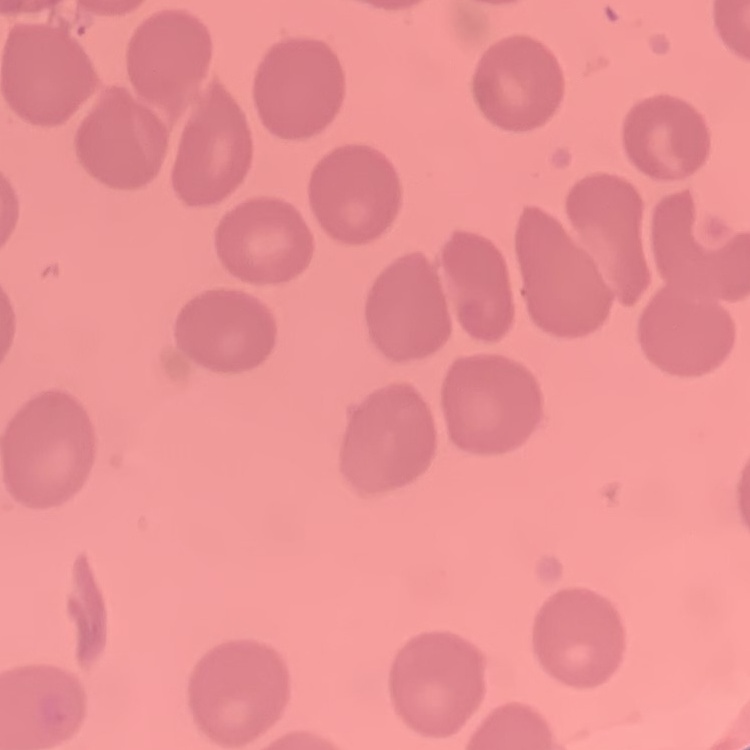
The erythrocytes show no rouleaux formation. Stained with either Field's or Giemsa. Thin blood smear. One tile cut from a larger photomicrograph.